Assess for malaria.
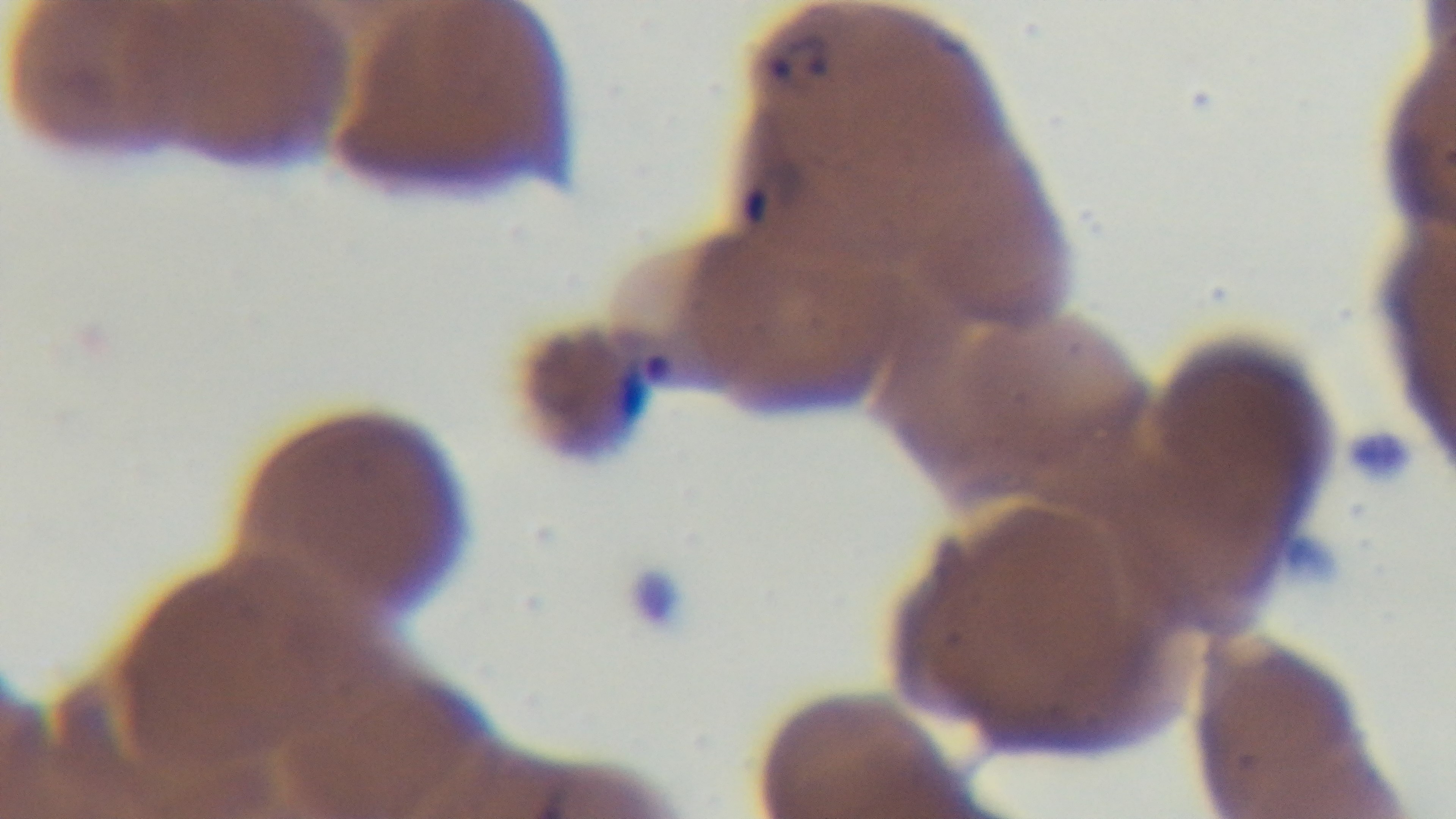

It is infected.

preparation = thin
stain = Giemsa
field of view = single
capture = mounted 4K digital camera
objective = 100x oil immersion
modality = light microscopy